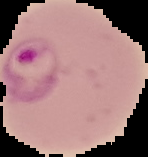

{
  "image_size": "148×157 pixels",
  "image_type": "cell region segmented out of the field of view; surrounding area masked to black",
  "preparation": "thin blood film",
  "malaria_status": "parasitized"
}